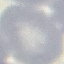

result: negative for malaria parasites
image_type: automatically extracted cell patch, resized to 64 × 64 pixels
preparation: thin blood smear
stain: Giemsa
capture: smartphone camera at the microscope eyepiece